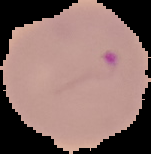
image_size: 151×154 pixels
preparation: thin blood smear
result: Plasmodium parasites detected
image_type: cell region segmented out of the field of view; surrounding area masked to black